Identify the parasite.
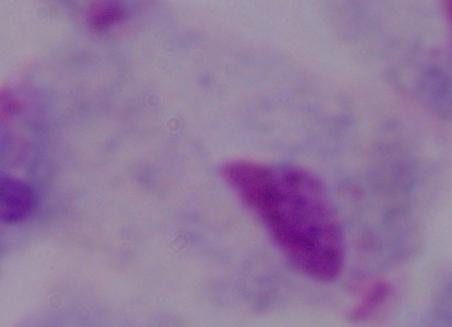
This is a trichomonad.

Photomicrograph. 1000x magnification.